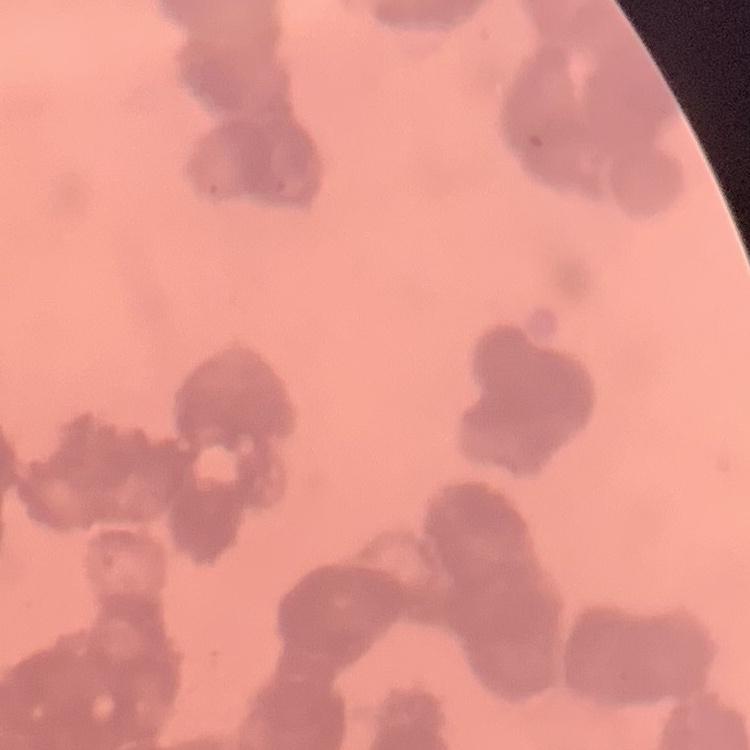
The erythrocytes exhibit rouleaux formation. Thin blood film. Field's or Giemsa stain. Square crop of a larger photomicrograph.